Comment on the morphology of the erythrocytes.
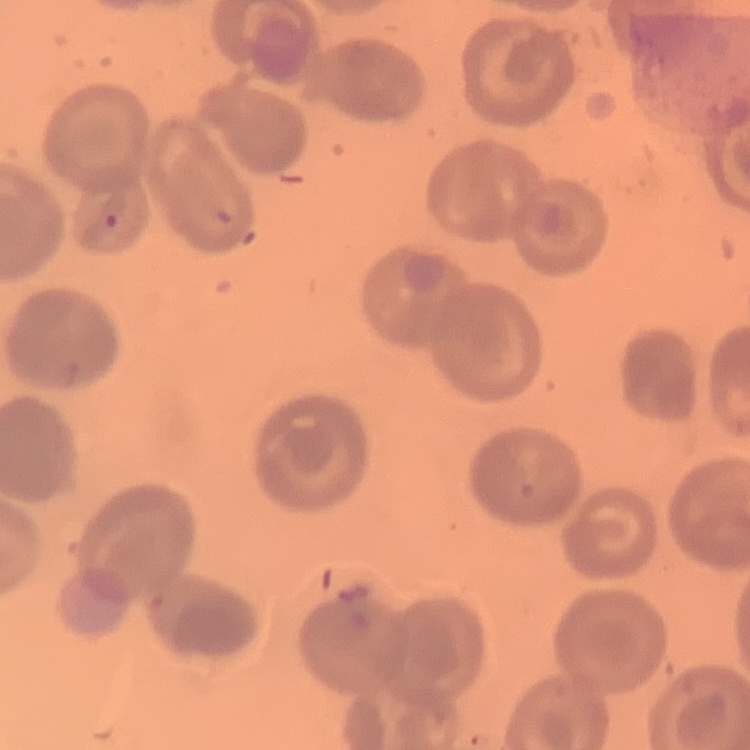

They show no rouleaux formation.

One tile cut from a larger photomicrograph. Field's or Giemsa stain. Thin blood film.